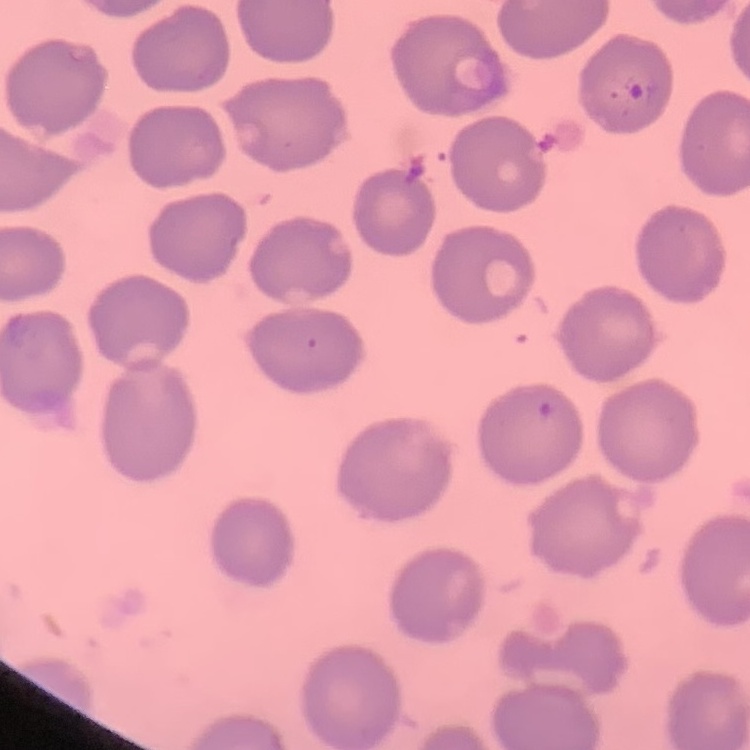
The red blood cells show no rouleaux formation. Thin peripheral smear. Square crop of a larger photomicrograph. Stained with either Field's or Giemsa.